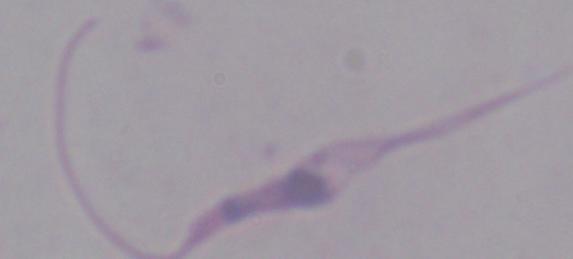
{
  "identification": "Leishmania",
  "modality": "micrograph",
  "magnification": "1000x"
}